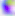

modality: micrograph
identification: Toxoplasma gondii
magnification: 400x